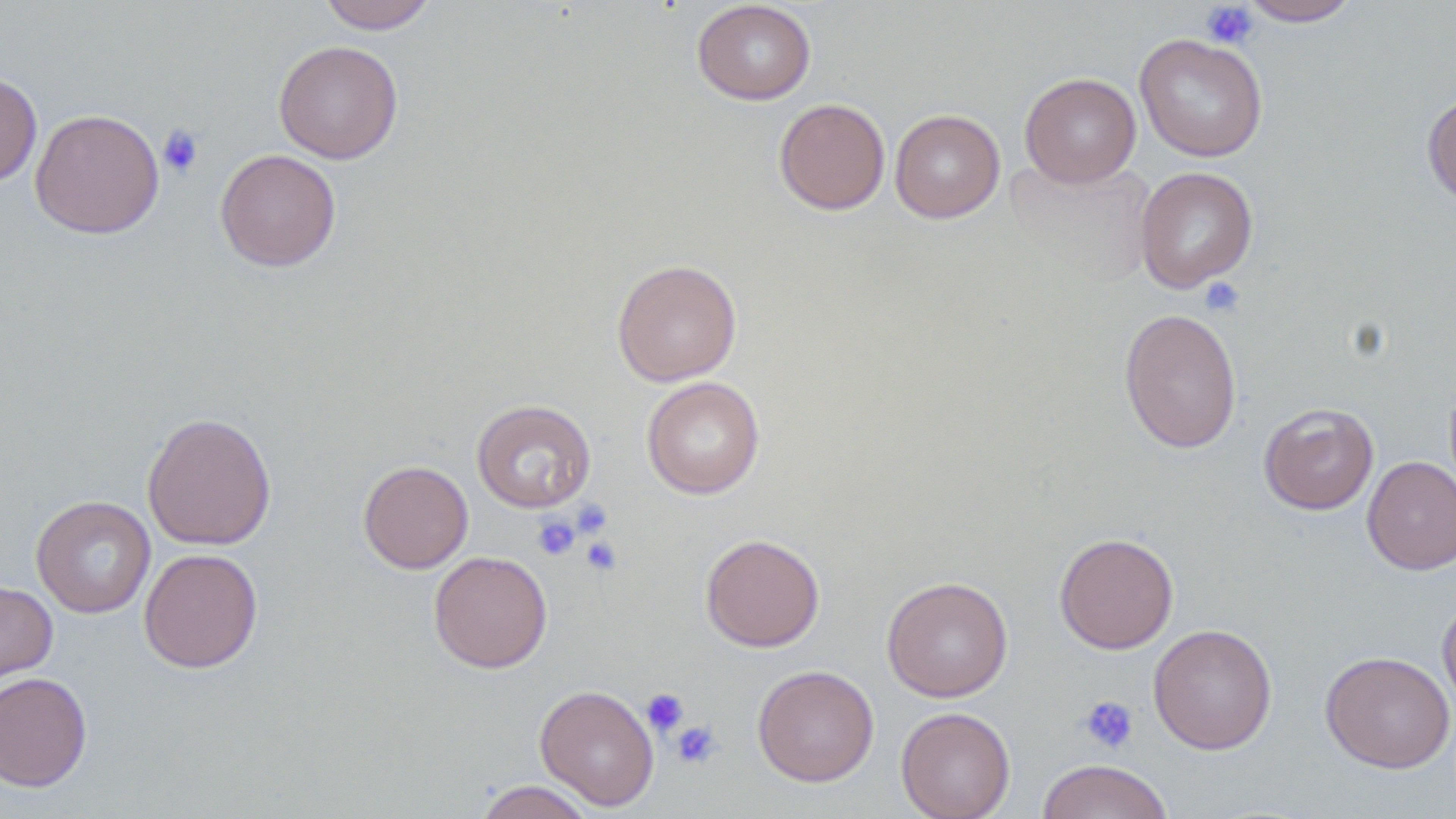
Summary:
  - Coordinate format: approximate bounding boxes as (x1,y1)-(x2,y2) corner pairs in pixels
  - Platelet locations: (1200,1)-(1258,49), (157,124)-(204,178), (1199,277)-(1245,318), (570,498)-(613,539), (531,514)-(581,561), (579,534)-(624,577), (641,688)-(689,737), (1078,695)-(1140,754), (669,719)-(722,770)
  - Uninfected red blood cell locations: (317,0)-(438,34), (1237,0)-(1361,26), (691,1)-(816,105), (1134,33)-(1268,162), (273,40)-(403,164), (0,72)-(42,187), (1019,72)-(1141,187), (1422,92)-(1456,209), (774,98)-(890,215), (29,108)-(164,239), (889,109)-(1005,223), (215,149)-(342,272), (1002,156)-(1156,292), (1135,167)-(1258,293), (612,258)-(742,386), (1118,307)-(1242,454), (641,377)-(765,499), (471,399)-(596,513), (1259,402)-(1379,515), (142,412)-(277,551), (1362,455)-(1456,574), (358,460)-(474,573), (31,495)-(156,618), (1054,532)-(1179,654), (700,533)-(825,652), (139,548)-(263,673), (429,551)-(552,673), (881,575)-(1013,702), (0,579)-(58,692), (1437,592)-(1456,719), (1148,623)-(1277,754), (1320,650)-(1455,773), (752,665)-(879,787), (0,671)-(92,792), (535,684)-(660,811), (896,707)-(1015,819), (1036,759)-(1174,819), (472,780)-(597,818)
  - Slide-level diagnosis: no evidence of blood parasites
  - Modality: optical microscopy
  - Field of view: single
  - Image size: 1456×819 pixels
  - Magnification: 1000x
  - Stain: May-Grünwald-Giemsa
  - Preparation: thin blood smear